Name the parasite shown.
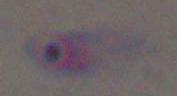

Toxoplasma gondii.

{
  "modality": "micrograph",
  "magnification": "1000x"
}